Identify the preparation type.
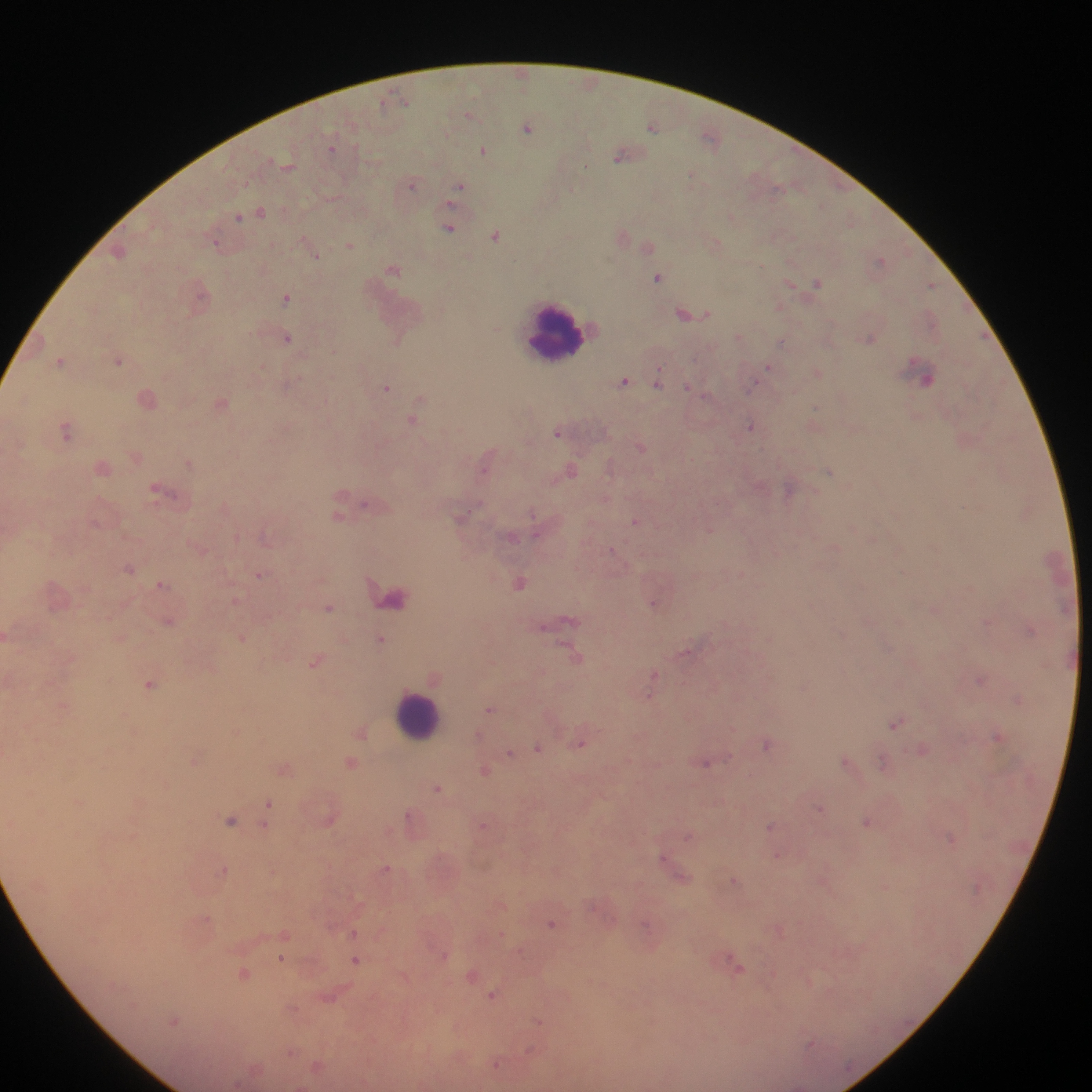
Thick blood film.

Approximate centers as (x, y) in pixels.
Summary:
  - Leukocyte locations: (554, 330), (414, 715)
  - Malaria parasite locations: (521, 71), (405, 100), (382, 102), (469, 114), (651, 127), (526, 129), (709, 135), (333, 148), (483, 151), (621, 157), (585, 167), (245, 183), (412, 186), (460, 187), (776, 187), (261, 211), (239, 217), (449, 228), (496, 236), (215, 243), (351, 244), (648, 247), (316, 254), (879, 260), (393, 270), (657, 278), (817, 282), (930, 284), (789, 285), (286, 298), (780, 305), (689, 316), (932, 319), (287, 337), (739, 337), (782, 341), (398, 343), (119, 360), (262, 366), (769, 366), (661, 367), (818, 371), (660, 374), (929, 378), (624, 380), (754, 383), (659, 384), (688, 386), (387, 387), (222, 403), (814, 408), (413, 420), (751, 426), (66, 431), (557, 433), (640, 447), (187, 462), (830, 472), (341, 499), (365, 505), (533, 514), (338, 516), (635, 522), (710, 528), (611, 550), (129, 568), (260, 576), (522, 582), (161, 584), (392, 596), (236, 599), (654, 605), (330, 607), (169, 621), (989, 622), (545, 627), (242, 637), (380, 639), (568, 649), (686, 652), (576, 658), (316, 662), (654, 674), (980, 680), (149, 684), (649, 696), (1017, 701), (64, 706), (488, 709), (125, 712), (897, 723), (733, 727), (361, 733), (998, 735), (580, 743), (767, 745), (538, 747), (922, 749), (509, 754), (846, 759), (882, 761), (196, 762), (350, 763), (705, 763), (283, 770), (484, 770), (437, 787), (74, 803), (268, 803), (821, 810), (409, 815), (229, 821), (867, 822), (264, 824), (483, 825), (771, 825), (688, 837), (952, 839), (776, 855), (664, 857), (386, 867), (225, 868), (733, 879), (884, 886), (207, 918), (552, 923), (354, 932), (287, 934), (501, 934), (520, 952), (445, 955), (728, 957), (282, 959), (356, 959), (741, 969), (244, 973), (472, 976), (811, 981), (492, 994), (294, 1008), (174, 1020), (539, 1020), (812, 1043), (530, 1048), (292, 1052), (498, 1065)
  - Image size: 1092×1092 pixels
  - Country: Ghana
  - Field of view: single
  - Capture: mobile-phone photograph through a microscope